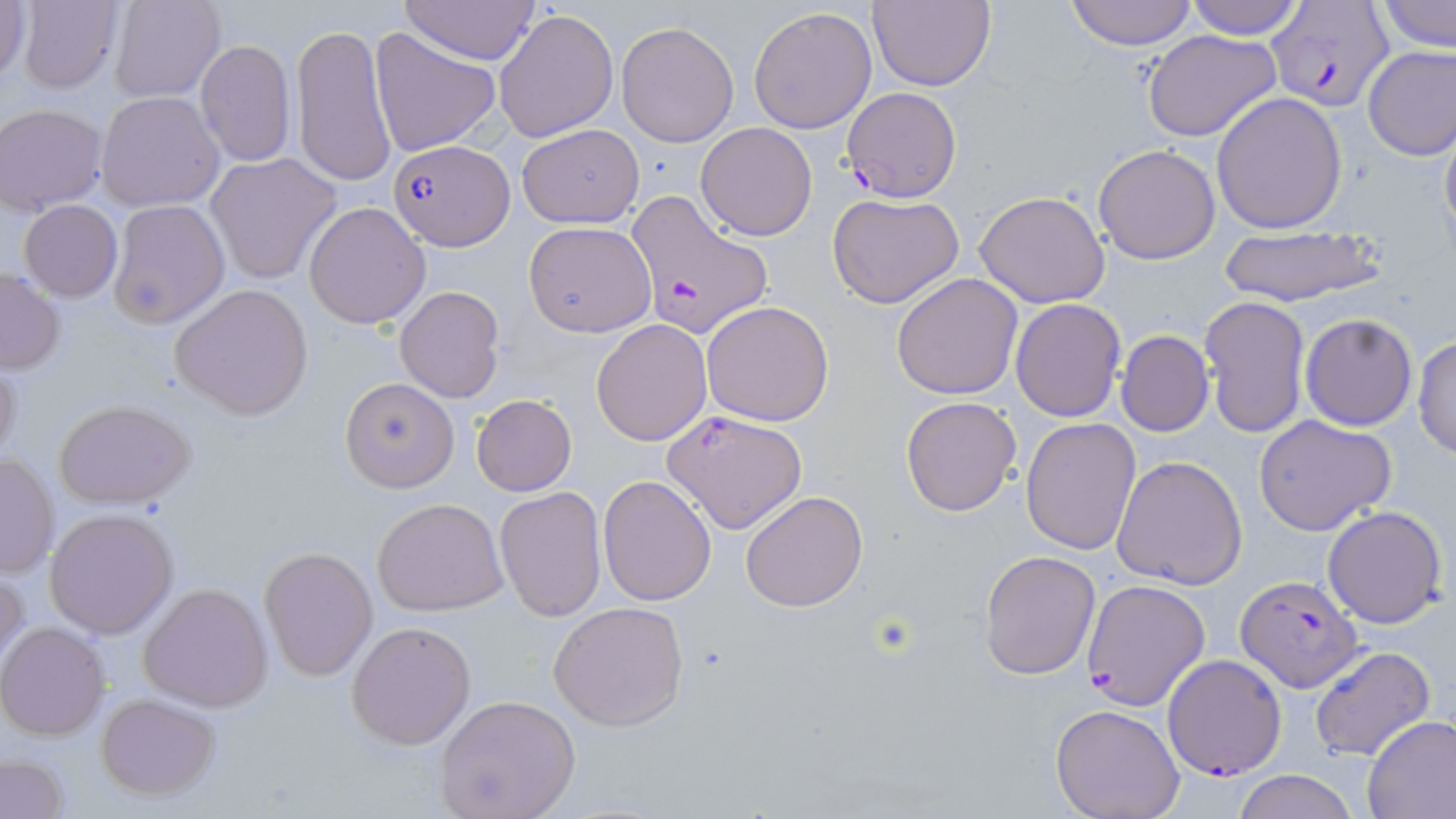
slide-level diagnosis = Plasmodium falciparum
magnification = 1000x
image size = 1456×819 pixels
Plasmodium falciparum-infected red blood cell locations = approximate bounding boxes as (x1,y1)-(x2,y2) corner pairs in pixels: (1268,3)-(1394,112), (839,88)-(961,202), (388,141)-(512,250), (625,192)-(774,339), (1235,574)-(1362,691), (1081,580)-(1211,710), (1160,654)-(1288,780)
field of view = single
stain = May-Grünwald-Giemsa
uninfected red blood cell locations = approximate bounding boxes as (x1,y1)-(x2,y2) corner pairs in pixels: (0,0)-(31,86), (15,0)-(124,94), (396,0)-(541,66), (1062,0)-(1201,48), (1181,0)-(1308,39), (1377,0)-(1455,54), (107,1)-(226,103), (866,1)-(996,90), (748,6)-(877,136), (493,7)-(618,144), (617,21)-(739,146), (291,22)-(397,188), (369,27)-(503,157), (1141,29)-(1283,142), (194,39)-(295,169), (1362,45)-(1456,162), (141,76)-(289,198), (95,92)-(224,212), (1211,92)-(1349,233), (1,103)-(108,214), (1438,110)-(1456,245), (696,122)-(818,240), (517,124)-(643,228), (1092,143)-(1222,265), (205,153)-(344,286), (974,190)-(1112,309), (827,193)-(966,309), (108,199)-(230,329), (19,200)-(122,302), (303,202)-(432,329), (523,220)-(656,337), (1213,225)-(1388,309), (1,265)-(65,375), (891,273)-(1024,400), (170,283)-(313,420), (395,286)-(505,402), (1198,296)-(1311,440), (1009,299)-(1126,421), (701,300)-(835,427), (1299,314)-(1417,429), (590,319)-(712,445), (1115,330)-(1214,438), (1413,333)-(1456,461), (0,355)-(22,473), (340,378)-(459,492), (471,395)-(577,495), (901,396)-(1021,517), (56,399)-(196,509), (661,409)-(809,535), (1254,415)-(1397,536), (1021,418)-(1142,556), (1,452)-(60,579), (1112,455)-(1247,590), (597,475)-(717,607), (495,484)-(607,622), (740,490)-(868,612), (373,496)-(508,616), (1322,505)-(1449,629), (45,508)-(179,638), (259,546)-(378,681), (979,549)-(1101,681), (0,563)-(28,676), (139,583)-(272,711), (548,601)-(689,730), (346,621)-(476,750), (0,622)-(110,741), (1309,645)-(1436,763), (95,692)-(222,802), (433,695)-(581,819), (1047,703)-(1186,819), (1360,714)-(1456,817), (1,753)-(68,817), (1229,769)-(1359,819)
modality = optical microscopy
preparation = thin blood film